Report the malaria status of this cell.
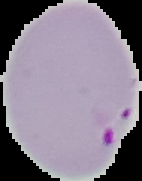
It is parasitized.

Segmented cell region on a black background. From a thin blood smear. Image is 142×181 pixels.